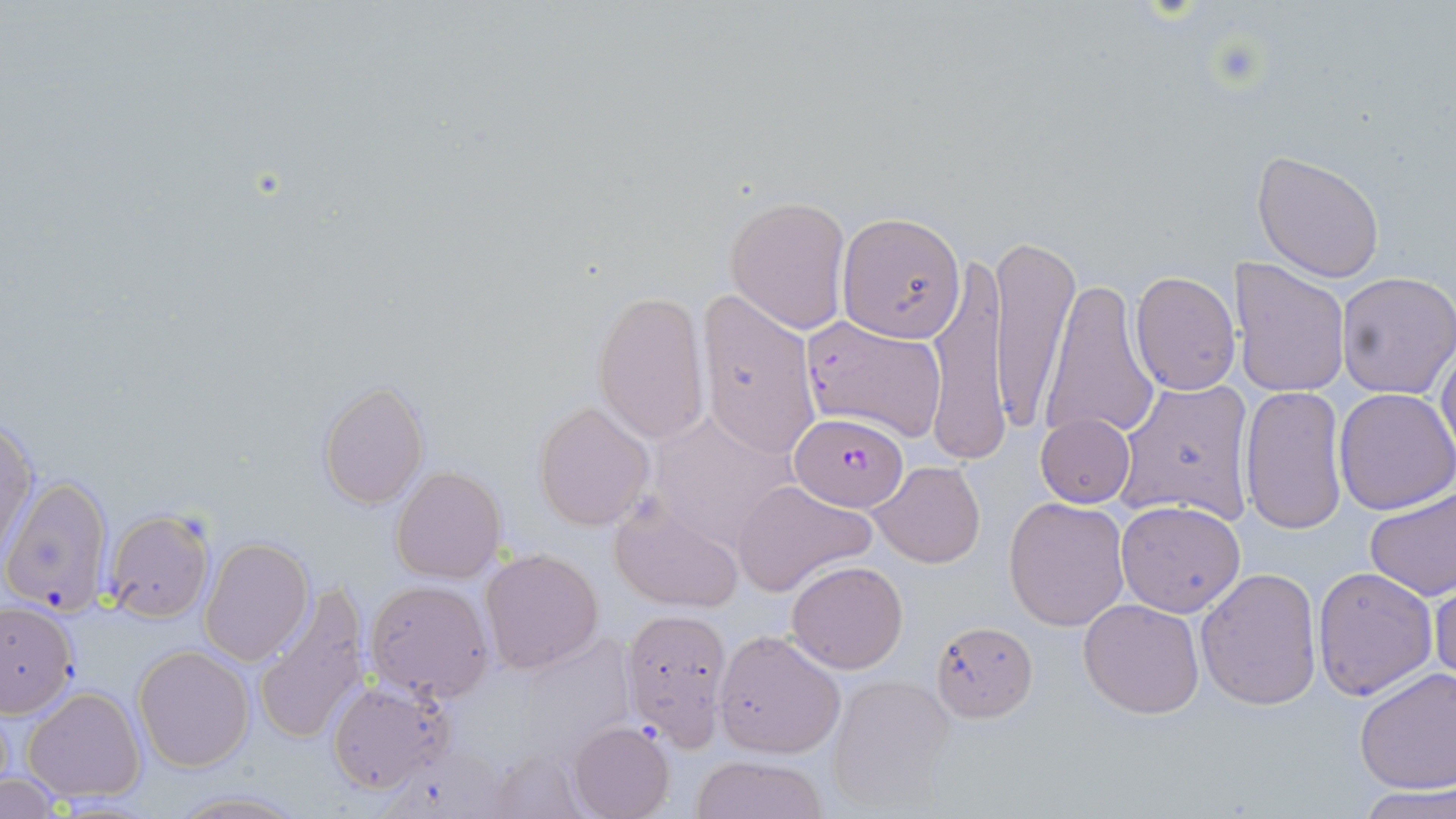 Approximate bounding boxes as (x1, y1, x2, y2) in pixels. Plasmodium falciparum-infected red blood cell locations: (800, 312, 945, 442), (789, 412, 908, 510). Uninfected red blood cell locations: (1252, 150, 1386, 282), (726, 196, 850, 332), (837, 212, 963, 345), (991, 233, 1078, 434), (927, 254, 1008, 463), (1230, 259, 1350, 398), (1334, 270, 1456, 398), (1129, 271, 1240, 394), (1040, 281, 1158, 444), (698, 287, 821, 462), (591, 289, 709, 443), (1437, 333, 1456, 466), (1113, 378, 1255, 524), (317, 379, 429, 508), (1240, 384, 1347, 536), (1333, 388, 1456, 514), (533, 401, 653, 531), (647, 409, 800, 551), (1, 414, 37, 562), (1036, 414, 1136, 508), (870, 460, 986, 568), (392, 467, 506, 584), (2, 475, 116, 616), (731, 479, 875, 594), (1364, 483, 1456, 602), (1003, 496, 1130, 631), (1115, 499, 1246, 618), (611, 501, 744, 613), (104, 508, 215, 624), (201, 535, 312, 665), (479, 549, 605, 675), (785, 560, 907, 674), (1310, 565, 1437, 699), (1196, 566, 1324, 710), (1431, 569, 1456, 686), (364, 579, 494, 701), (740, 582, 876, 726), (255, 584, 373, 745), (1078, 598, 1204, 719), (0, 600, 78, 717), (621, 608, 731, 748), (930, 619, 1037, 721), (715, 628, 845, 758), (133, 645, 253, 771), (1355, 666, 1456, 793), (827, 673, 958, 814), (327, 678, 457, 793), (22, 686, 146, 803), (569, 720, 674, 819), (482, 745, 590, 819), (691, 753, 828, 819), (0, 774, 65, 816), (1357, 787, 1456, 819), (168, 790, 305, 818). Slide-level diagnosis: Plasmodium falciparum. Thin blood film. May-Grünwald-Giemsa-stained preparation. One field of a larger specimen. 1000x magnification. Image is 1456×819 pixels. Optical microscopy.